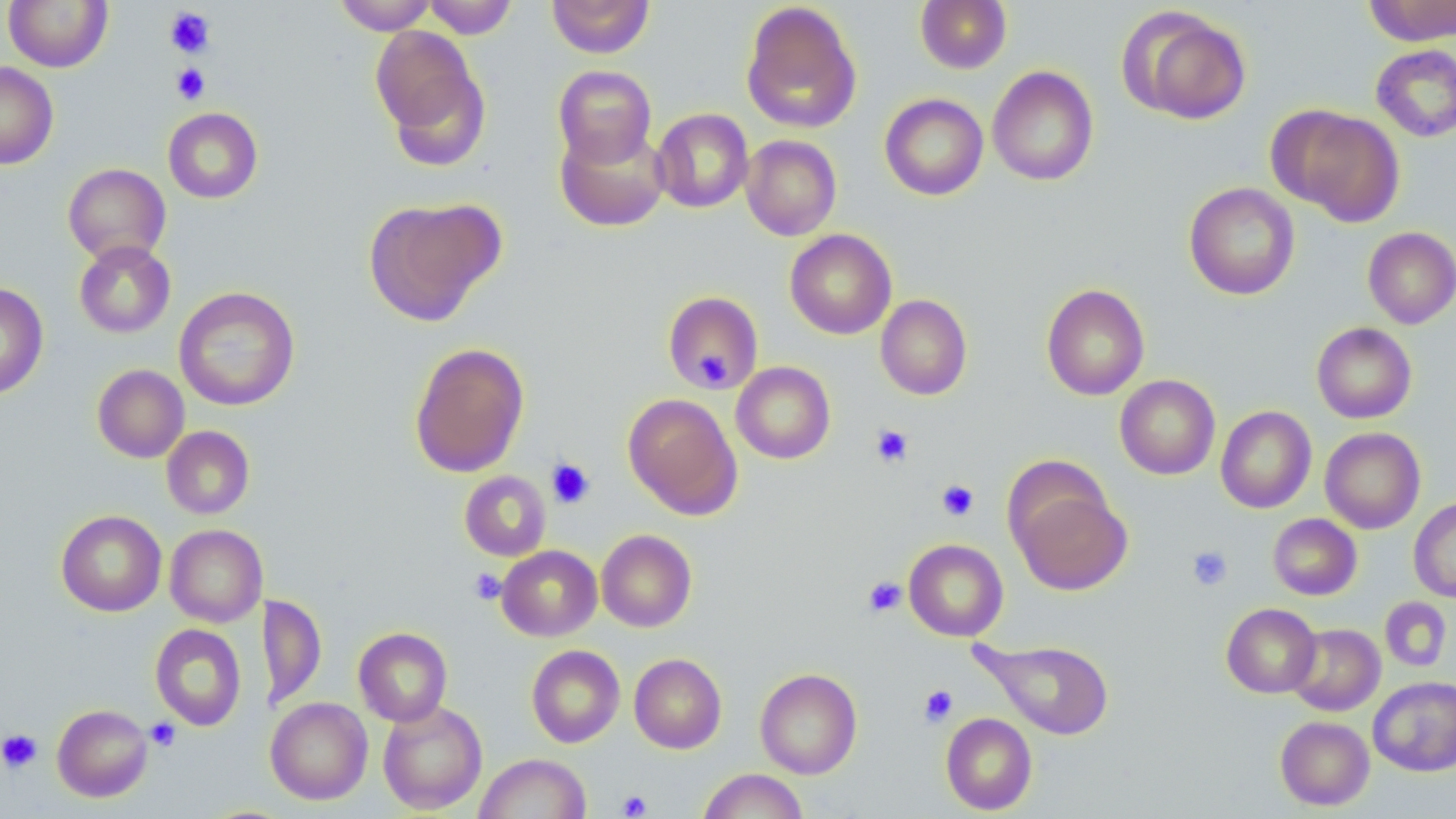

slide-level diagnosis = no evidence of blood parasites
image size = 1456×819 pixels
uninfected red blood cell locations = approximate bounding boxes as (x1,y1)-(x2,y2) corner pairs in pixels: (3,0)-(113,72), (334,0)-(437,34), (423,0)-(518,39), (547,0)-(655,58), (915,0)-(1012,73), (1361,1)-(1455,46), (741,2)-(862,134), (1121,7)-(1252,125), (371,25)-(489,160), (1371,44)-(1456,142), (0,62)-(59,169), (553,65)-(657,167), (987,66)-(1099,186), (880,93)-(989,200), (1272,105)-(1405,225), (162,107)-(263,203), (652,108)-(754,213), (556,124)-(670,232), (741,135)-(841,240), (63,163)-(171,265), (1184,182)-(1300,300), (363,197)-(505,326), (1363,227)-(1456,328), (785,229)-(897,340), (74,240)-(176,338), (0,282)-(48,398), (1041,283)-(1149,401), (174,286)-(300,412), (662,290)-(764,394), (875,295)-(972,400), (1311,322)-(1417,423), (409,341)-(529,478), (731,361)-(835,464), (92,364)-(189,463), (1115,375)-(1220,480), (623,393)-(742,519), (1216,406)-(1316,514), (161,426)-(255,519), (1320,427)-(1426,533), (459,471)-(551,561), (1011,481)-(1132,596), (1409,497)-(1456,603), (56,510)-(167,616), (1268,513)-(1362,600), (165,524)-(266,627), (596,529)-(697,632), (904,539)-(1008,641), (497,545)-(602,641), (261,594)-(326,710), (1379,597)-(1452,672), (1221,603)-(1321,698), (150,623)-(247,731), (1286,623)-(1385,715), (353,627)-(453,726), (978,638)-(1116,740), (526,645)-(625,748), (629,653)-(726,753), (755,668)-(862,779), (1368,676)-(1456,776), (265,697)-(373,804), (378,700)-(488,815), (52,704)-(153,802), (940,713)-(1038,815), (1274,716)-(1374,810), (474,753)-(592,818), (698,768)-(808,819)
platelet locations = approximate bounding boxes as (x1,y1)-(x2,y2) corner pairs in pixels: (164,7)-(215,58), (171,64)-(210,104), (698,347)-(729,384), (871,424)-(914,468), (546,458)-(595,509), (936,479)-(979,522), (1187,545)-(1233,591), (469,569)-(506,604), (863,576)-(907,617), (918,684)-(958,727), (145,718)-(181,751), (0,728)-(43,773), (617,789)-(652,817)
modality = light microscopy
magnification = 1000x
preparation = thin blood smear
field of view = single
stain = May-Grünwald-Giemsa